Name the blood parasite species.
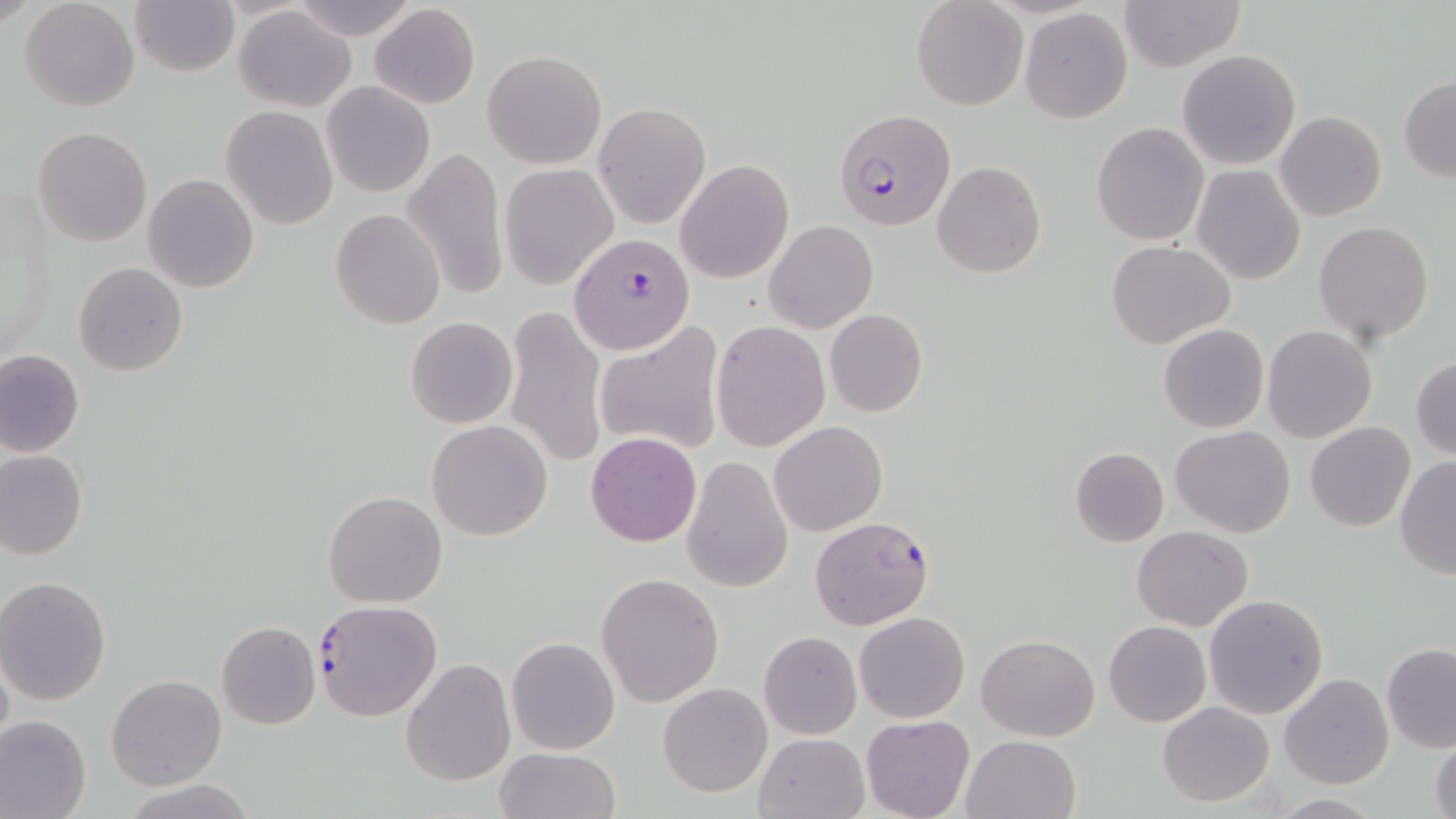
Plasmodium falciparum.

Summary:
  - Coordinate format: approximate bounding boxes as (x1, y1, x2, y2) in pixels
  - Uninfected red blood cell locations: (20, 0, 140, 112), (130, 0, 240, 77), (1119, 0, 1246, 71), (290, 1, 417, 39), (911, 1, 1027, 111), (368, 4, 479, 111), (234, 6, 356, 111), (1019, 8, 1133, 124), (1177, 49, 1301, 171), (483, 50, 605, 169), (1398, 75, 1456, 181), (322, 81, 436, 198), (594, 102, 710, 229), (221, 107, 337, 228), (1276, 111, 1387, 223), (1092, 121, 1210, 246), (33, 127, 152, 248), (401, 146, 509, 302), (676, 160, 794, 283), (933, 162, 1046, 278), (500, 164, 616, 289), (1191, 166, 1305, 284), (143, 173, 261, 292), (331, 209, 445, 328), (764, 220, 878, 334), (1314, 221, 1435, 345), (1106, 239, 1235, 348), (72, 261, 188, 377), (503, 304, 608, 469), (825, 309, 928, 418), (405, 317, 517, 429), (593, 320, 726, 458), (712, 322, 829, 450), (1159, 323, 1269, 433), (1261, 325, 1376, 442), (0, 350, 84, 457), (1411, 355, 1456, 459), (770, 420, 888, 536), (427, 421, 551, 540), (1305, 422, 1414, 531), (1170, 426, 1295, 536), (586, 431, 702, 548), (1068, 448, 1168, 548), (0, 451, 88, 559), (1394, 456, 1456, 580), (682, 457, 793, 593), (322, 491, 449, 608), (1134, 526, 1253, 630), (596, 572, 724, 706), (1, 575, 115, 706), (1203, 594, 1329, 719), (855, 611, 970, 723), (216, 621, 321, 730), (1104, 621, 1211, 727), (758, 631, 861, 739), (977, 633, 1098, 742), (506, 637, 621, 755), (1382, 642, 1456, 753), (0, 649, 13, 753), (402, 658, 514, 786), (1279, 674, 1393, 789), (106, 676, 227, 791), (658, 683, 772, 797), (1157, 702, 1275, 805), (0, 714, 91, 819), (861, 714, 975, 819), (753, 732, 871, 819), (959, 733, 1081, 819), (1430, 733, 1456, 819), (494, 746, 620, 819), (125, 780, 254, 819)
  - Plasmodium falciparum-infected red blood cell locations: (836, 108, 954, 231), (570, 233, 694, 354), (809, 515, 934, 631), (311, 600, 441, 722)
  - Stain: May-Grünwald-Giemsa
  - Modality: optical microscopy
  - Preparation: thin blood film
  - Field of view: single
  - Magnification: 1000x
  - Image size: 1456×819 pixels